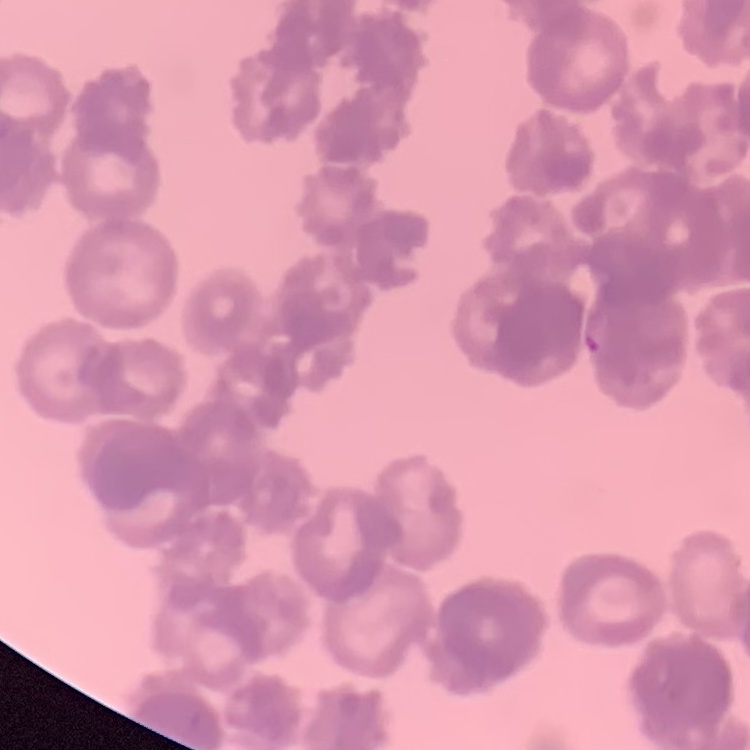
Summary:
  - Erythrocyte morphology: rouleaux formation
  - Preparation: thin peripheral smear
  - Image type: square crop of a larger photomicrograph
  - Stain: Field's or Giemsa